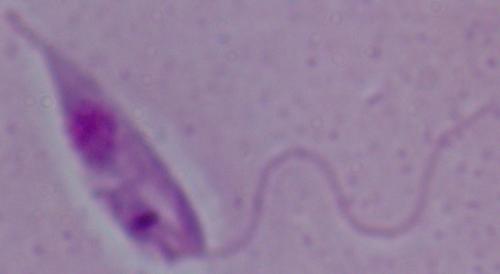 Micrograph. Captured at 1000x magnification. A Leishmania parasite is shown.